Give the extent of all Plasmodium vivax-infected red blood cells.
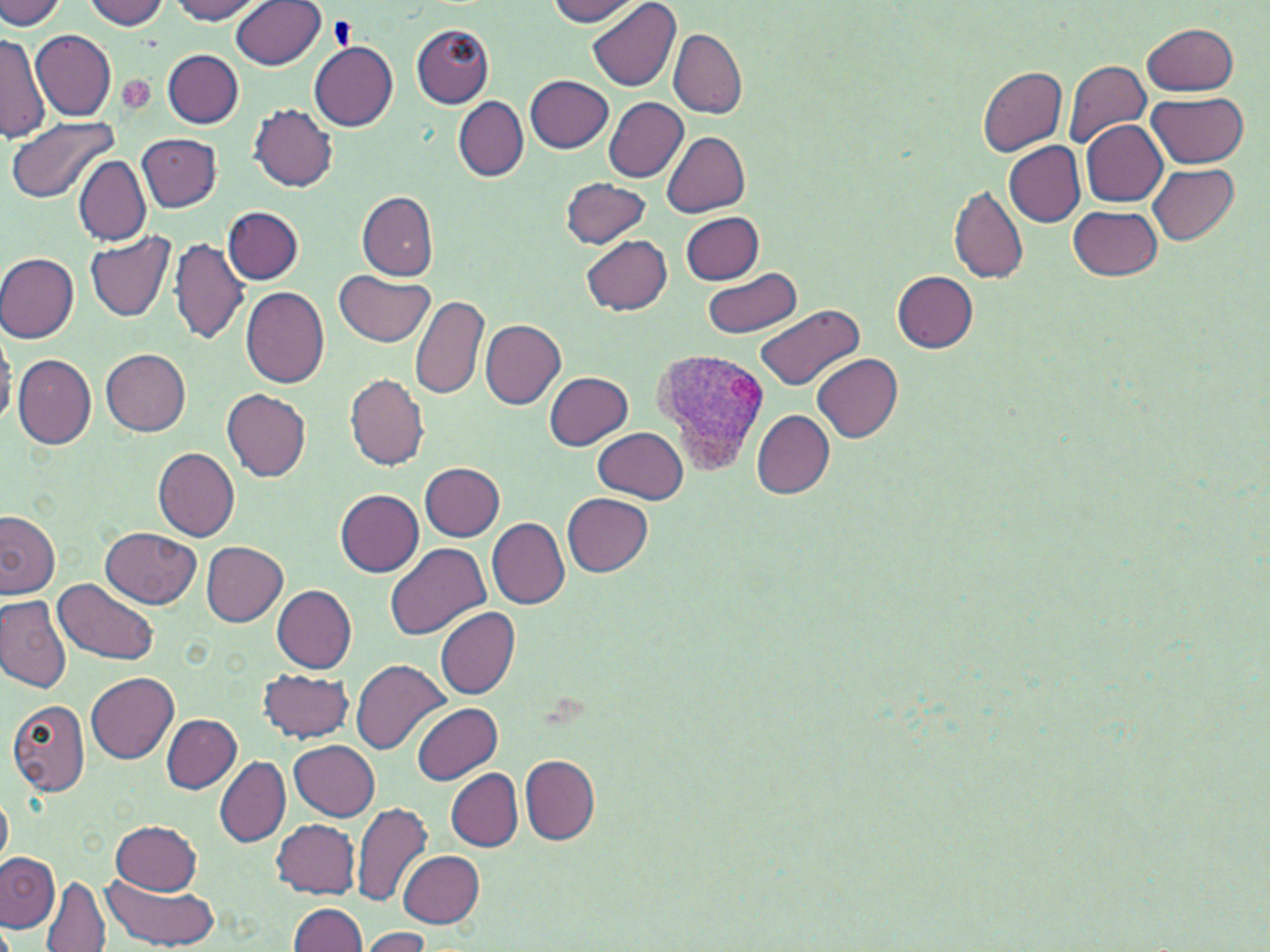
Approximate bounding boxes as (x1, y1, x2, y2) in pixels.
Plasmodium vivax-infected red blood cells: (654, 348, 772, 471).

Uninfected red blood cell locations: (0, 0, 67, 29), (170, 0, 265, 24), (547, 0, 644, 25), (587, 0, 683, 91), (83, 1, 170, 29), (232, 2, 325, 69), (1143, 22, 1238, 95), (412, 23, 494, 107), (31, 29, 115, 121), (669, 29, 746, 118), (0, 31, 49, 145), (309, 40, 398, 131), (161, 50, 245, 128), (1064, 58, 1151, 149), (977, 66, 1067, 156), (526, 75, 613, 153), (1146, 93, 1249, 167), (453, 96, 527, 181), (604, 97, 689, 182), (249, 103, 338, 192), (6, 118, 116, 202), (1080, 119, 1168, 205), (661, 129, 749, 216), (138, 132, 221, 211), (1003, 141, 1085, 226), (74, 155, 149, 246), (1149, 163, 1241, 244), (570, 173, 659, 312), (561, 177, 652, 248), (950, 184, 1026, 284), (357, 191, 438, 280), (223, 205, 304, 284), (1069, 206, 1163, 280), (680, 211, 764, 285), (85, 230, 176, 322), (582, 235, 672, 314), (169, 238, 249, 345), (0, 252, 79, 343), (701, 266, 802, 340), (336, 270, 435, 345), (891, 271, 978, 352), (240, 287, 331, 388), (411, 296, 489, 400), (756, 305, 863, 391), (480, 320, 565, 408), (0, 323, 17, 428), (102, 349, 192, 436), (10, 353, 190, 445), (14, 354, 96, 449), (813, 354, 902, 441), (344, 372, 429, 471), (544, 372, 634, 450), (221, 389, 313, 481), (750, 409, 834, 498), (595, 427, 689, 504), (153, 448, 240, 543), (420, 463, 505, 541), (334, 489, 424, 576), (562, 493, 653, 576), (0, 512, 60, 598), (488, 518, 570, 608), (101, 526, 201, 607), (200, 540, 288, 626), (385, 542, 491, 642), (55, 577, 161, 666), (271, 585, 357, 673), (0, 596, 72, 692), (436, 607, 520, 698), (352, 658, 450, 754), (259, 668, 354, 743), (86, 672, 179, 765), (8, 700, 90, 797), (413, 701, 501, 785), (162, 714, 241, 793), (290, 740, 379, 821), (520, 755, 600, 844), (214, 756, 289, 847), (446, 770, 523, 851), (0, 793, 11, 869), (352, 802, 431, 908), (111, 820, 202, 893), (274, 820, 360, 898), (397, 850, 484, 926), (0, 851, 59, 934), (102, 873, 222, 949), (39, 875, 111, 952), (289, 902, 368, 952), (363, 927, 432, 951). Platelet locations: (328, 18, 352, 50). Slide-level diagnosis: Plasmodium vivax. Image is 1270×952 pixels. One field of a larger specimen. Light microscopy. Thin blood film. 1000x magnification. May-Grünwald-Giemsa-stained preparation.